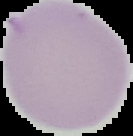
Summary:
  - Image type: segmented cell region with the area outside set to black
  - Result: negative for Plasmodium parasites
  - Image size: 133×136 pixels
  - Preparation: thin blood smear